Locate every Plasmodium falciparum-infected red blood cell.
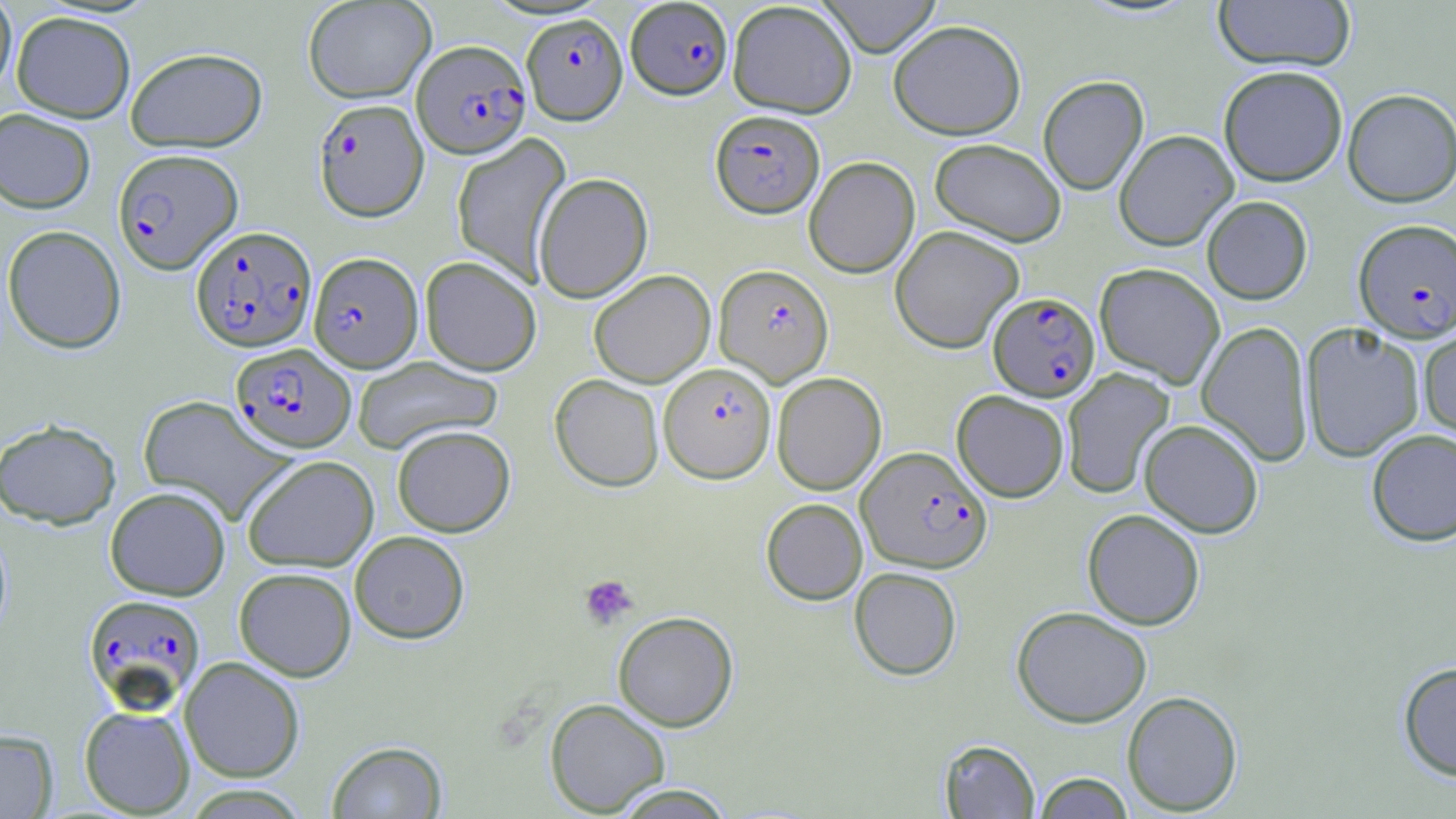

Approximate bounding boxes as (x1, y1, x2, y2) in pixels.
Plasmodium falciparum-infected red blood cells: (626, 0, 733, 99), (522, 13, 627, 124), (412, 40, 530, 157), (313, 98, 429, 221), (710, 109, 824, 218), (113, 148, 242, 274), (1353, 219, 1456, 341), (191, 225, 316, 352), (308, 252, 423, 372), (714, 263, 834, 386), (988, 292, 1099, 401), (231, 343, 356, 452), (659, 362, 776, 482), (856, 445, 991, 573), (83, 593, 206, 713).

Summary:
  - Platelet locations: (579, 574, 639, 630)
  - Uninfected red blood cell locations: (0, 0, 17, 97), (302, 0, 436, 103), (817, 0, 942, 57), (728, 1, 857, 118), (1214, 1, 1356, 72), (11, 11, 135, 123), (888, 19, 1026, 140), (125, 47, 268, 152), (1218, 65, 1348, 186), (1038, 75, 1148, 195), (1343, 88, 1456, 206), (0, 108, 96, 213), (1114, 129, 1238, 250), (451, 133, 572, 286), (930, 138, 1067, 247), (804, 156, 920, 278), (533, 172, 653, 303), (1202, 196, 1312, 304), (1, 224, 127, 354), (890, 225, 1025, 353), (420, 256, 541, 376), (1095, 262, 1225, 388), (589, 270, 715, 388), (1196, 321, 1314, 467), (1301, 323, 1424, 463), (1418, 325, 1456, 445), (353, 356, 502, 454), (1061, 369, 1174, 498), (772, 372, 886, 494), (550, 374, 664, 491), (952, 390, 1069, 502), (138, 395, 295, 524), (0, 419, 121, 529), (1139, 419, 1264, 538), (392, 424, 515, 537), (1366, 429, 1456, 546), (241, 455, 379, 572), (105, 486, 231, 600), (761, 498, 868, 604), (1082, 508, 1205, 630), (349, 530, 469, 644), (234, 567, 356, 681), (849, 567, 962, 680), (1012, 606, 1152, 727), (613, 611, 738, 731), (179, 656, 305, 783), (1397, 661, 1456, 781), (1122, 690, 1243, 815), (545, 698, 671, 816), (79, 705, 195, 817), (0, 728, 59, 819), (939, 739, 1039, 818), (326, 740, 448, 818), (1034, 772, 1133, 818), (608, 784, 737, 818)
  - Slide-level diagnosis: Plasmodium falciparum
  - Stain: May-Grünwald-Giemsa
  - Modality: light microscopy
  - Magnification: 1000x
  - Image size: 1456×819 pixels
  - Preparation: thin blood smear
  - Field of view: one of a larger specimen